Locate every blood parasite and identify its species.
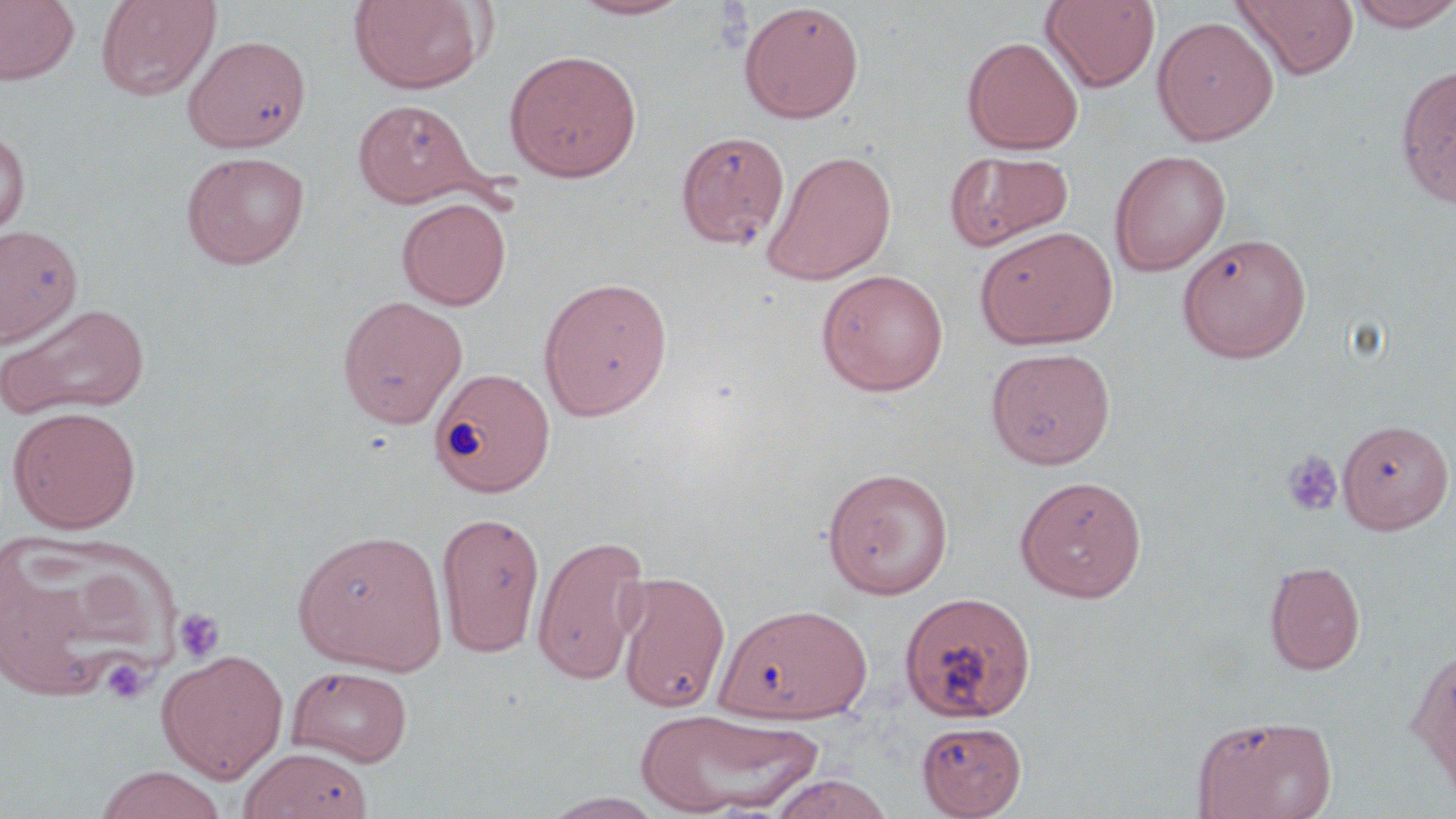
No blood parasites observed.

Approximate bounding boxes as named x1/y1/x2/y2 corners in pixels. Uninfected red blood cell locations: (x1=0, y1=0, x2=80, y2=86), (x1=95, y1=0, x2=222, y2=100), (x1=348, y1=0, x2=490, y2=95), (x1=567, y1=0, x2=695, y2=21), (x1=1040, y1=0, x2=1161, y2=92), (x1=1232, y1=0, x2=1359, y2=79), (x1=1345, y1=0, x2=1456, y2=31), (x1=739, y1=3, x2=864, y2=123), (x1=1152, y1=15, x2=1279, y2=146), (x1=183, y1=35, x2=311, y2=152), (x1=962, y1=36, x2=1083, y2=154), (x1=505, y1=49, x2=643, y2=182), (x1=1395, y1=64, x2=1456, y2=207), (x1=352, y1=99, x2=480, y2=207), (x1=0, y1=129, x2=31, y2=235), (x1=676, y1=130, x2=791, y2=250), (x1=761, y1=148, x2=898, y2=285), (x1=944, y1=150, x2=1074, y2=252), (x1=1110, y1=150, x2=1231, y2=275), (x1=181, y1=151, x2=310, y2=269), (x1=397, y1=197, x2=511, y2=310), (x1=0, y1=225, x2=83, y2=348), (x1=975, y1=226, x2=1119, y2=349), (x1=1178, y1=233, x2=1311, y2=363), (x1=816, y1=269, x2=949, y2=396), (x1=537, y1=276, x2=673, y2=421), (x1=336, y1=294, x2=468, y2=428), (x1=0, y1=302, x2=151, y2=420), (x1=986, y1=348, x2=1116, y2=468), (x1=430, y1=367, x2=555, y2=496), (x1=7, y1=406, x2=141, y2=533), (x1=1338, y1=420, x2=1454, y2=533), (x1=821, y1=467, x2=954, y2=599), (x1=1015, y1=475, x2=1147, y2=601), (x1=436, y1=511, x2=545, y2=658), (x1=292, y1=528, x2=448, y2=675), (x1=0, y1=532, x2=180, y2=705), (x1=532, y1=534, x2=650, y2=685), (x1=1264, y1=560, x2=1366, y2=675), (x1=613, y1=570, x2=731, y2=712), (x1=899, y1=591, x2=1036, y2=724), (x1=715, y1=602, x2=873, y2=724), (x1=1408, y1=644, x2=1455, y2=801), (x1=157, y1=648, x2=289, y2=783), (x1=286, y1=664, x2=413, y2=767), (x1=635, y1=707, x2=822, y2=816), (x1=1193, y1=714, x2=1337, y2=819), (x1=916, y1=720, x2=1027, y2=818), (x1=239, y1=747, x2=373, y2=819), (x1=91, y1=766, x2=229, y2=819), (x1=768, y1=773, x2=895, y2=819), (x1=542, y1=792, x2=668, y2=818). Platelet locations: (x1=1282, y1=451, x2=1343, y2=517), (x1=172, y1=607, x2=225, y2=665), (x1=101, y1=657, x2=153, y2=705). Slide-level diagnosis: negative for blood parasites. Optical microscopy. Image is 1456×819 pixels. May-Grünwald-Giemsa stain. Thin blood smear. 1000x magnification. Single field of view.